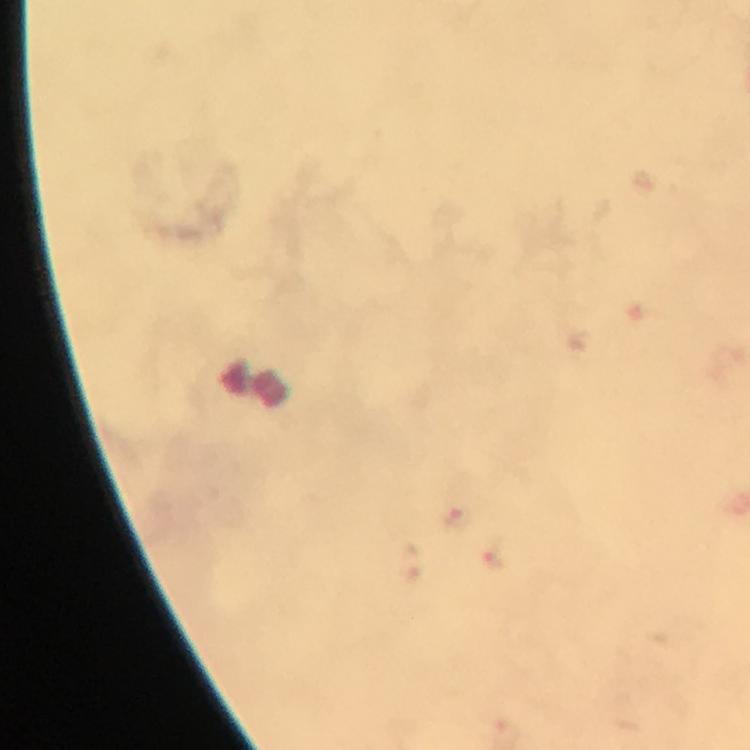

Approximate centers as {x, y} in pixels.
Summary:
  - Malaria parasite locations: {459, 517}, {496, 558}
  - Preparation: thick blood film
  - Context: from a malaria diagnostic workup
  - Stain: Giemsa
  - Image size: 750×750 pixels
  - Capture: smartphone mounted on the microscope
  - Cropped from: one field of view
  - Immersion oil: used
  - Magnification: 100x